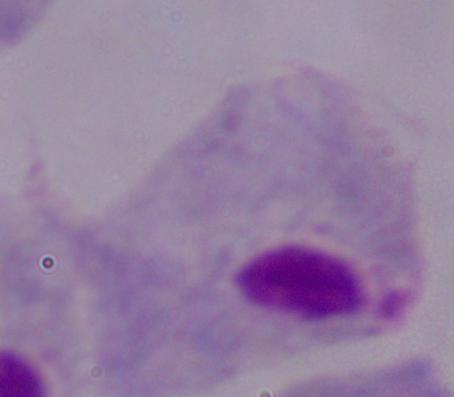

A trichomonad is shown. 1000x magnification. Micrograph.